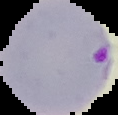

Cell region segmented out of the field of view; the surrounding area is masked to black. Result: Plasmodium parasites identified. From a thin blood film. Image is 118×115 pixels.